Outline each Plasmodium ovale-infected red blood cell.
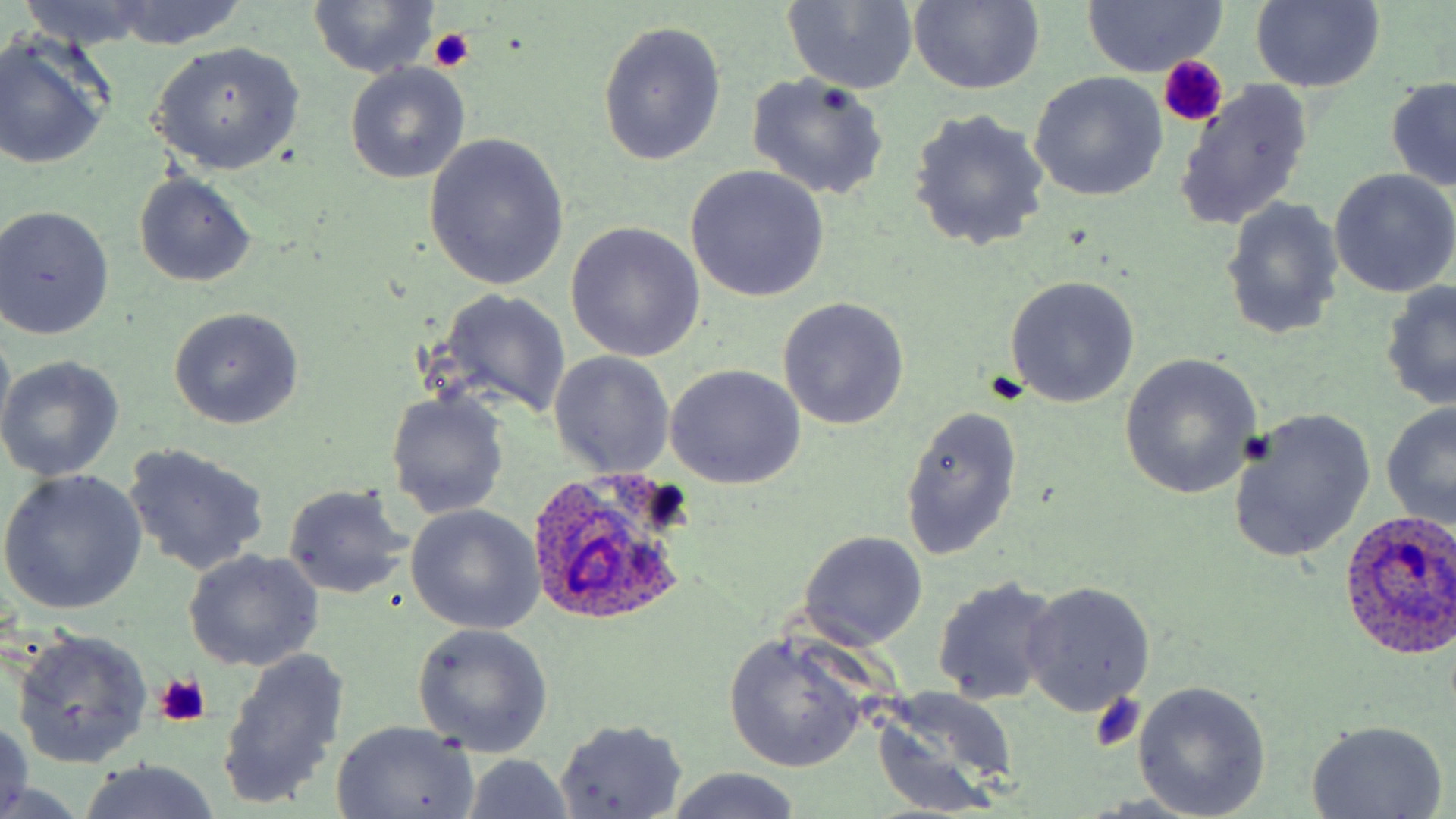
Approximate bounding boxes as (x1, y1, x2, y2) in pixels.
Plasmodium ovale-infected red blood cells: (527, 469, 690, 621), (1337, 513, 1456, 661).

slide-level diagnosis = Plasmodium ovale
uninfected red blood cell locations = approximate bounding boxes as (x1, y1, x2, y2) in pixels: (1249, 0, 1385, 92), (17, 1, 163, 49), (104, 1, 251, 51), (907, 1, 1043, 97), (1082, 1, 1225, 75), (307, 2, 443, 78), (780, 2, 920, 93), (597, 20, 726, 166), (0, 38, 113, 169), (149, 41, 305, 177), (344, 63, 470, 183), (1029, 72, 1168, 200), (745, 73, 890, 199), (1384, 77, 1456, 193), (1174, 80, 1316, 233), (908, 107, 1051, 254), (423, 134, 570, 293), (684, 166, 829, 302), (1328, 169, 1456, 298), (133, 174, 256, 287), (1220, 198, 1344, 341), (0, 205, 115, 338), (566, 223, 704, 362), (1004, 275, 1140, 409), (1381, 280, 1456, 412), (429, 288, 572, 420), (777, 298, 908, 430), (167, 307, 304, 428), (0, 321, 15, 442), (547, 352, 675, 478), (0, 354, 124, 481), (1119, 354, 1264, 501), (666, 365, 806, 489), (384, 389, 509, 519), (1381, 404, 1456, 529), (898, 405, 1024, 562), (1228, 408, 1375, 563), (122, 444, 270, 576), (0, 470, 148, 615), (281, 484, 411, 599), (406, 505, 544, 634), (799, 531, 928, 651), (183, 549, 325, 672), (931, 575, 1064, 706), (1020, 582, 1155, 717), (411, 624, 552, 758), (10, 630, 152, 767), (723, 635, 868, 773), (218, 646, 350, 811), (1132, 680, 1272, 818), (869, 690, 1018, 812), (0, 718, 33, 819), (552, 719, 687, 818), (1302, 719, 1449, 819), (331, 721, 479, 818), (459, 755, 579, 819), (76, 760, 223, 819), (664, 769, 803, 819)
field of view = one of a larger specimen
magnification = 1000x
stain = May-Grünwald-Giemsa
modality = light microscopy
image size = 1456×819 pixels
platelet locations = approximate bounding boxes as (x1, y1, x2, y2) in pixels: (428, 26, 474, 72), (1157, 55, 1227, 128), (155, 672, 213, 727), (1088, 694, 1146, 752)
preparation = thin blood smear